Report the malaria status of this cell.
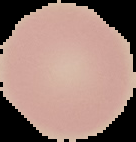

It is uninfected.

Image is 136×142 pixels. Segmented cell region on a black background. From a thin blood film.